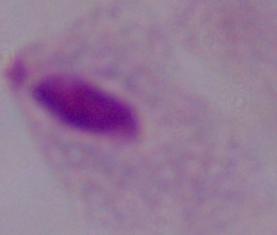
{
  "modality": "photomicrograph",
  "identification": "trichomonad",
  "magnification": "1000x"
}